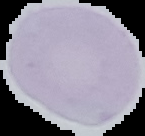
Summary:
  - Malaria status: uninfected
  - Preparation: thin blood film
  - Image size: 145×136 pixels
  - Image type: segmented cell region on a black background